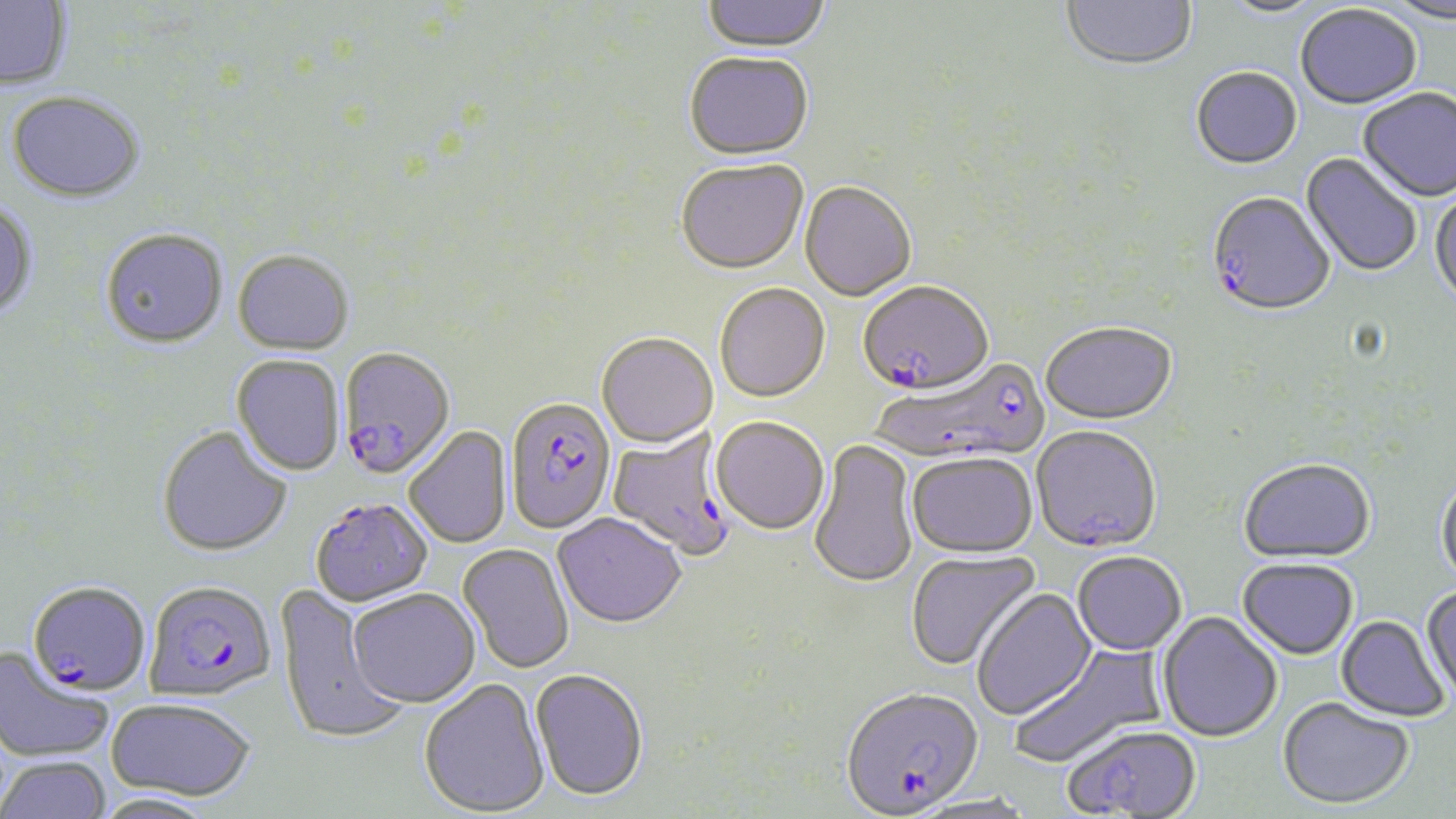

{
  "plasmodium_falciparum_infected_red_blood_cell_locations": "approximate bounding boxes as (x1,y1)-(x2,y2) corner pairs in pixels: (1207,192)-(1336,319), (858,279)-(993,395), (337,345)-(455,479), (872,355)-(1051,466), (505,395)-(617,533), (608,428)-(738,561), (309,497)-(433,606), (144,579)-(277,700), (28,581)-(151,696), (841,685)-(983,815)",
  "slide_level_diagnosis": "Plasmodium falciparum",
  "field_of_view": "one of a larger specimen",
  "magnification": "1000x",
  "image_size": "1456×819 pixels",
  "modality": "light microscopy",
  "stain": "May-Grünwald-Giemsa",
  "uninfected_red_blood_cell_locations": "approximate bounding boxes as (x1,y1)-(x2,y2) corner pairs in pixels: (701,0)-(831,54), (1061,0)-(1198,73), (1383,0)-(1456,26), (0,1)-(72,91), (1217,1)-(1328,20), (1295,7)-(1422,111), (683,51)-(815,159), (1191,69)-(1303,171), (1358,88)-(1456,203), (7,90)-(145,202), (1300,153)-(1422,278), (676,158)-(808,273), (800,180)-(916,301), (1429,189)-(1456,309), (0,202)-(38,319), (100,227)-(228,347), (233,248)-(354,354), (714,281)-(830,401), (1041,321)-(1177,424), (596,331)-(718,447), (232,354)-(345,476), (712,415)-(830,535), (1031,425)-(1161,551), (157,426)-(292,556), (404,426)-(511,548), (808,440)-(919,588), (907,452)-(1038,557), (1238,458)-(1375,563), (1436,472)-(1456,590), (553,512)-(686,627), (458,543)-(574,674), (905,550)-(1040,671), (1072,551)-(1186,655), (1238,557)-(1359,659), (276,584)-(407,745), (1422,585)-(1456,707), (970,586)-(1097,721), (348,588)-(479,707), (1157,611)-(1283,742), (1336,614)-(1450,723), (1008,643)-(1165,770), (0,648)-(113,763), (530,668)-(648,800), (419,678)-(550,817), (1277,696)-(1414,809), (105,697)-(256,801), (1061,722)-(1202,819), (0,756)-(111,819), (93,791)-(220,819)",
  "preparation": "thin blood film"
}